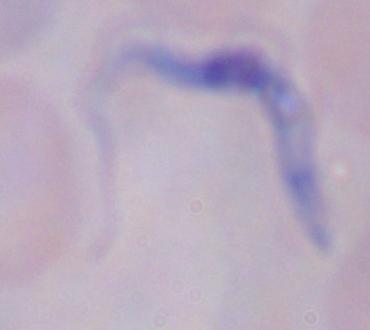

Summary:
  - Magnification: 1000x
  - Modality: micrograph
  - Identification: trypanosome